Locate every blood parasite and identify its species.
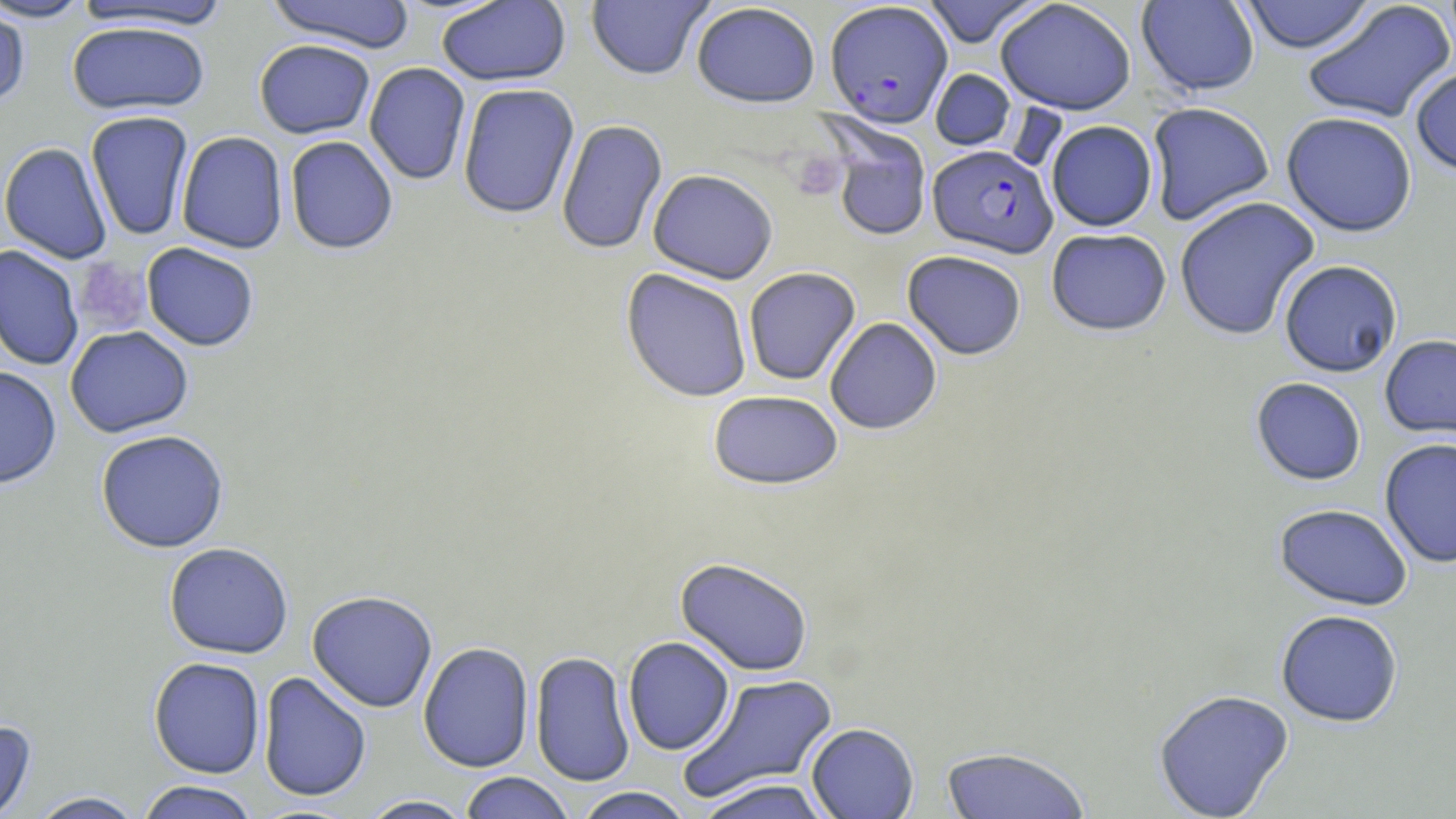
Approximate bounding boxes as named x1/y1/x2/y2 corners in pixels.
Plasmodium falciparum-infected red blood cells: (x1=824, y1=1, x2=953, y2=127), (x1=927, y1=144, x2=1057, y2=258).
No Plasmodium ovale, Plasmodium malariae, Plasmodium vivax, Babesia divergens, or Trypanosoma brucei observed.

slide-level diagnosis = Plasmodium falciparum
uninfected red blood cell locations = approximate bounding boxes as named x1/y1/x2/y2 corners in pixels: (x1=0, y1=0, x2=93, y2=23), (x1=265, y1=0, x2=416, y2=52), (x1=436, y1=0, x2=572, y2=86), (x1=585, y1=0, x2=713, y2=80), (x1=921, y1=0, x2=1044, y2=48), (x1=995, y1=0, x2=1137, y2=115), (x1=1136, y1=0, x2=1260, y2=97), (x1=1237, y1=0, x2=1377, y2=54), (x1=72, y1=1, x2=231, y2=32), (x1=1302, y1=1, x2=1456, y2=124), (x1=691, y1=2, x2=821, y2=108), (x1=0, y1=6, x2=31, y2=111), (x1=67, y1=20, x2=211, y2=115), (x1=254, y1=39, x2=375, y2=139), (x1=364, y1=62, x2=471, y2=186), (x1=1410, y1=66, x2=1456, y2=175), (x1=930, y1=69, x2=1016, y2=151), (x1=457, y1=83, x2=580, y2=219), (x1=1145, y1=102, x2=1275, y2=226), (x1=85, y1=110, x2=194, y2=241), (x1=1281, y1=112, x2=1418, y2=237), (x1=820, y1=115, x2=932, y2=242), (x1=556, y1=119, x2=668, y2=256), (x1=1046, y1=120, x2=1157, y2=232), (x1=176, y1=131, x2=288, y2=254), (x1=285, y1=136, x2=398, y2=255), (x1=0, y1=142, x2=112, y2=264), (x1=648, y1=168, x2=778, y2=284), (x1=1173, y1=196, x2=1321, y2=340), (x1=1046, y1=228, x2=1172, y2=336), (x1=141, y1=242, x2=260, y2=352), (x1=0, y1=245, x2=84, y2=371), (x1=902, y1=250, x2=1027, y2=360), (x1=1278, y1=259, x2=1403, y2=377), (x1=743, y1=267, x2=861, y2=386), (x1=621, y1=268, x2=753, y2=403), (x1=825, y1=317, x2=942, y2=435), (x1=65, y1=325, x2=194, y2=438), (x1=1379, y1=334, x2=1456, y2=441), (x1=0, y1=367, x2=62, y2=490), (x1=1251, y1=377, x2=1367, y2=486), (x1=708, y1=390, x2=844, y2=490), (x1=95, y1=429, x2=229, y2=553), (x1=1379, y1=438, x2=1456, y2=569), (x1=1274, y1=503, x2=1413, y2=611), (x1=164, y1=542, x2=294, y2=659), (x1=675, y1=557, x2=814, y2=676), (x1=307, y1=590, x2=438, y2=712), (x1=1275, y1=609, x2=1403, y2=728), (x1=623, y1=636, x2=735, y2=755), (x1=418, y1=642, x2=534, y2=773), (x1=530, y1=651, x2=635, y2=786), (x1=148, y1=657, x2=266, y2=779), (x1=257, y1=671, x2=372, y2=803), (x1=679, y1=672, x2=840, y2=802), (x1=1153, y1=688, x2=1294, y2=819), (x1=0, y1=720, x2=37, y2=819), (x1=806, y1=723, x2=919, y2=819), (x1=940, y1=746, x2=1091, y2=819), (x1=458, y1=772, x2=576, y2=819), (x1=693, y1=778, x2=835, y2=819), (x1=136, y1=781, x2=260, y2=819), (x1=570, y1=787, x2=694, y2=818), (x1=26, y1=791, x2=148, y2=818), (x1=359, y1=795, x2=476, y2=818)
platelet locations = approximate bounding boxes as named x1/y1/x2/y2 corners in pixels: (x1=791, y1=151, x2=845, y2=201), (x1=75, y1=259, x2=152, y2=335)
magnification = 1000x
field of view = one of a larger specimen
stain = May-Grünwald-Giemsa
image size = 1456×819 pixels
preparation = thin blood smear
modality = light microscopy